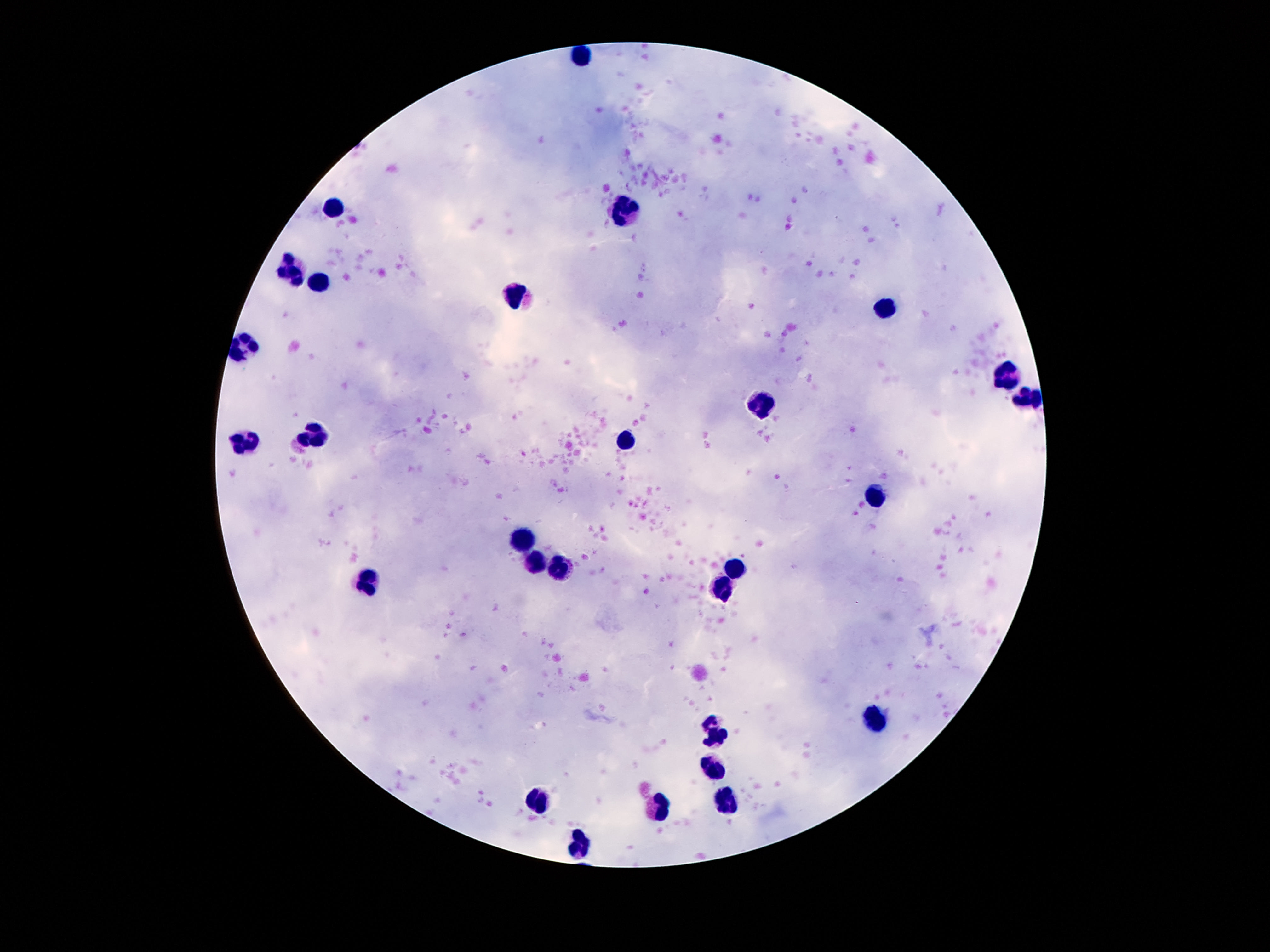

Approximate centers as (x, y) in pixels.
Summary:
  - Leukocyte locations: (584, 57), (332, 210), (627, 214), (293, 272), (321, 281), (513, 296), (886, 307), (240, 350), (1006, 376), (1030, 399), (758, 406), (313, 434), (625, 439), (244, 444), (877, 498), (522, 540), (541, 564), (735, 568), (561, 570), (369, 581), (718, 594), (873, 721), (717, 734), (711, 762), (537, 801), (722, 803), (657, 808), (580, 844)
  - Preparation: thick blood smear
  - Magnification: 100x
  - Field of view: one from this slide
  - Image size: 1270×952 pixels
  - Patient malaria status: negative
  - Capture: smartphone camera through the microscope eyepiece
  - Stain: Giemsa